Assess this cell for malaria.
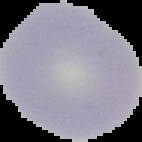

Uninfected.

Segmented cell region on a black background. From a thin blood smear. Image is 142×142 pixels.